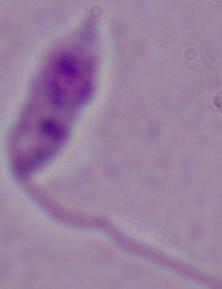

identification = Leishmania
modality = photomicrograph
magnification = 1000x